Locate platelets.
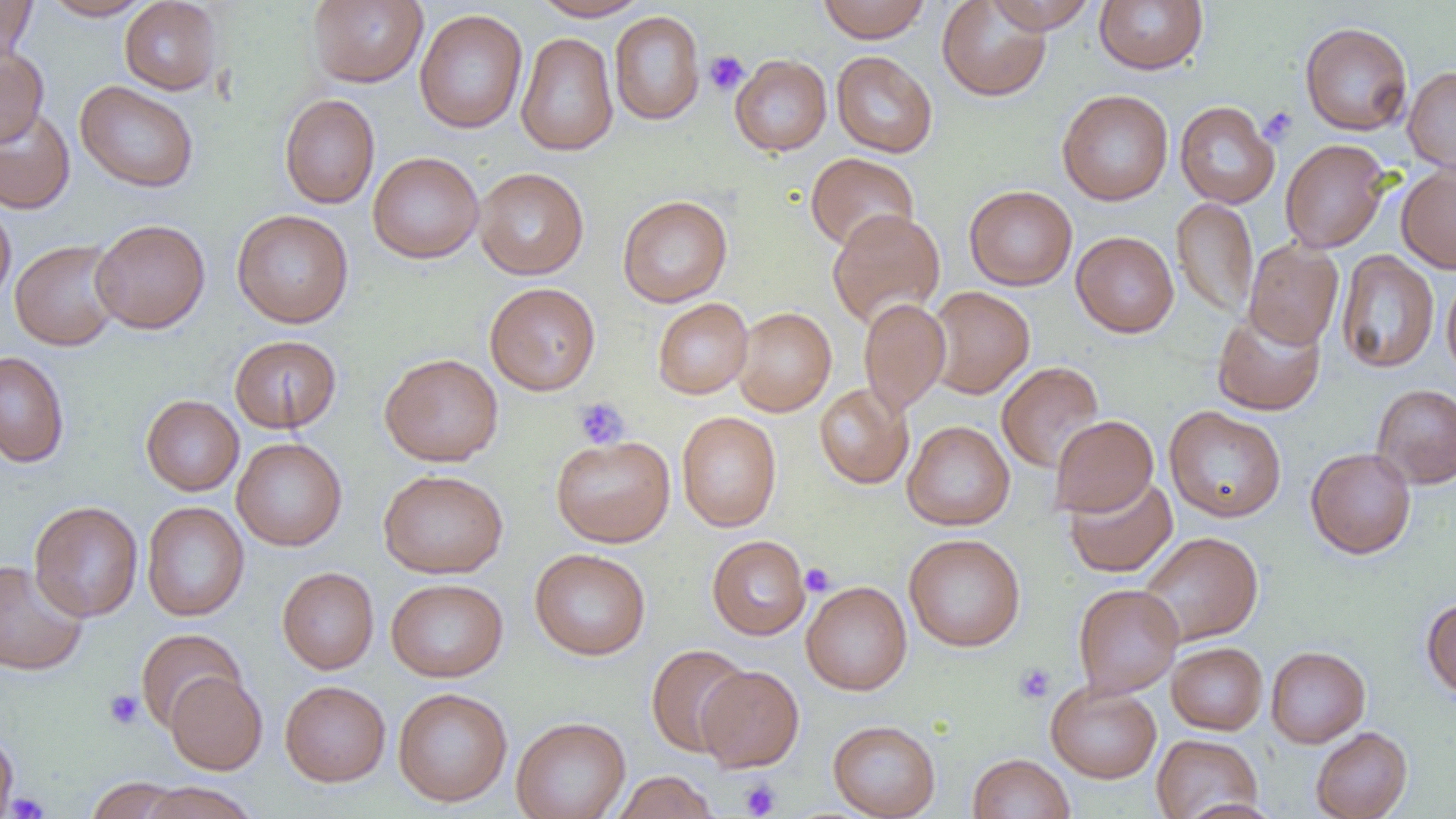

Approximate bounding boxes as [x1, y1, x2, y2] in pixels.
Platelets: [703, 50, 749, 96], [1258, 106, 1298, 146], [573, 397, 630, 450], [800, 563, 835, 596], [1014, 662, 1055, 704], [103, 689, 144, 730], [739, 778, 782, 818], [8, 790, 49, 818].

slide-level diagnosis = no evidence of blood parasites
preparation = thin blood film
field of view = single
magnification = 1000x
image size = 1456×819 pixels
modality = light microscopy
uninfected red blood cell locations = approximate bounding boxes as [x1, y1, x2, y2] in pixels: [0, 0, 37, 62], [41, 0, 153, 20], [307, 0, 428, 88], [530, 0, 651, 21], [818, 0, 930, 43], [1094, 0, 1208, 74], [119, 1, 222, 95], [936, 1, 1052, 102], [985, 1, 1097, 34], [414, 9, 528, 134], [609, 11, 705, 125], [1299, 21, 1413, 136], [515, 31, 618, 156], [0, 45, 49, 147], [831, 50, 938, 158], [730, 54, 832, 156], [1403, 65, 1456, 174], [75, 80, 199, 193], [1057, 89, 1173, 205], [279, 93, 380, 209], [1175, 101, 1280, 208], [0, 106, 76, 214], [1280, 139, 1391, 253], [368, 152, 484, 263], [805, 152, 919, 252], [1396, 163, 1456, 273], [474, 167, 589, 280], [964, 185, 1077, 291], [617, 195, 732, 307], [1171, 198, 1258, 319], [0, 203, 15, 308], [828, 208, 945, 330], [231, 209, 354, 328], [90, 218, 211, 334], [1071, 231, 1179, 338], [10, 239, 123, 351], [1243, 240, 1343, 349], [1336, 249, 1439, 374], [1441, 272, 1456, 384], [485, 282, 601, 395], [926, 286, 1034, 398], [653, 297, 753, 399], [859, 297, 950, 416], [733, 306, 836, 416], [1212, 307, 1326, 417], [229, 335, 342, 433], [0, 350, 70, 467], [379, 353, 504, 466], [996, 361, 1104, 473], [814, 383, 913, 489], [1371, 383, 1456, 489], [141, 395, 244, 496], [1163, 406, 1287, 522], [677, 411, 782, 532], [1049, 415, 1158, 517], [902, 420, 1015, 530], [551, 435, 675, 547], [232, 437, 347, 551], [1305, 447, 1416, 559], [378, 469, 508, 578], [1063, 473, 1177, 578], [29, 500, 143, 622], [141, 501, 249, 622], [1137, 531, 1263, 647], [904, 533, 1026, 651], [707, 535, 811, 640], [530, 548, 651, 660], [0, 560, 89, 675], [277, 567, 379, 674], [386, 578, 508, 682], [801, 580, 912, 695], [1073, 583, 1183, 698], [1422, 597, 1456, 702], [136, 628, 246, 732], [1167, 642, 1268, 734], [646, 644, 752, 757], [1266, 646, 1370, 747], [696, 665, 804, 772], [166, 671, 267, 774], [280, 680, 391, 786], [1046, 681, 1161, 783], [393, 687, 512, 807], [511, 715, 631, 819], [828, 719, 941, 819], [1310, 727, 1412, 819], [0, 729, 19, 819], [1151, 733, 1262, 818], [968, 753, 1075, 819], [611, 771, 719, 819], [85, 777, 187, 818], [136, 782, 260, 819], [1179, 798, 1283, 819]